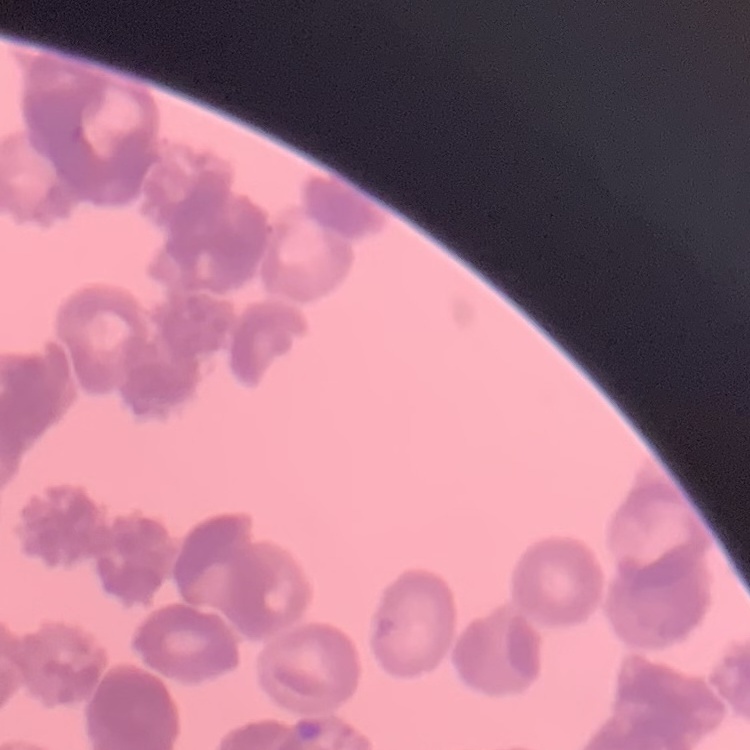
{
  "erythrocyte_morphology": "rouleaux formation",
  "image_type": "square crop of a larger photomicrograph",
  "stain": "Field's or Giemsa",
  "preparation": "thin blood film"
}